Report the malaria status of this cell.
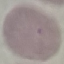

Uninfected.

preparation = thin smear
capture = smartphone through the microscope eyepiece
stain = Giemsa
image type = automatically extracted cell patch, resized to 64 × 64 pixels